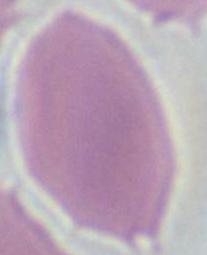

Summary:
  - Modality: micrograph
  - Magnification: 1000x
  - Identification: red blood cell